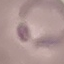

Malaria status: parasitized. Acquired by smartphone through the microscope eyepiece. Giemsa-stained preparation. Thin blood smear. Cell patch, automatically extracted from a larger field of view and resized to 64 × 64 pixels.